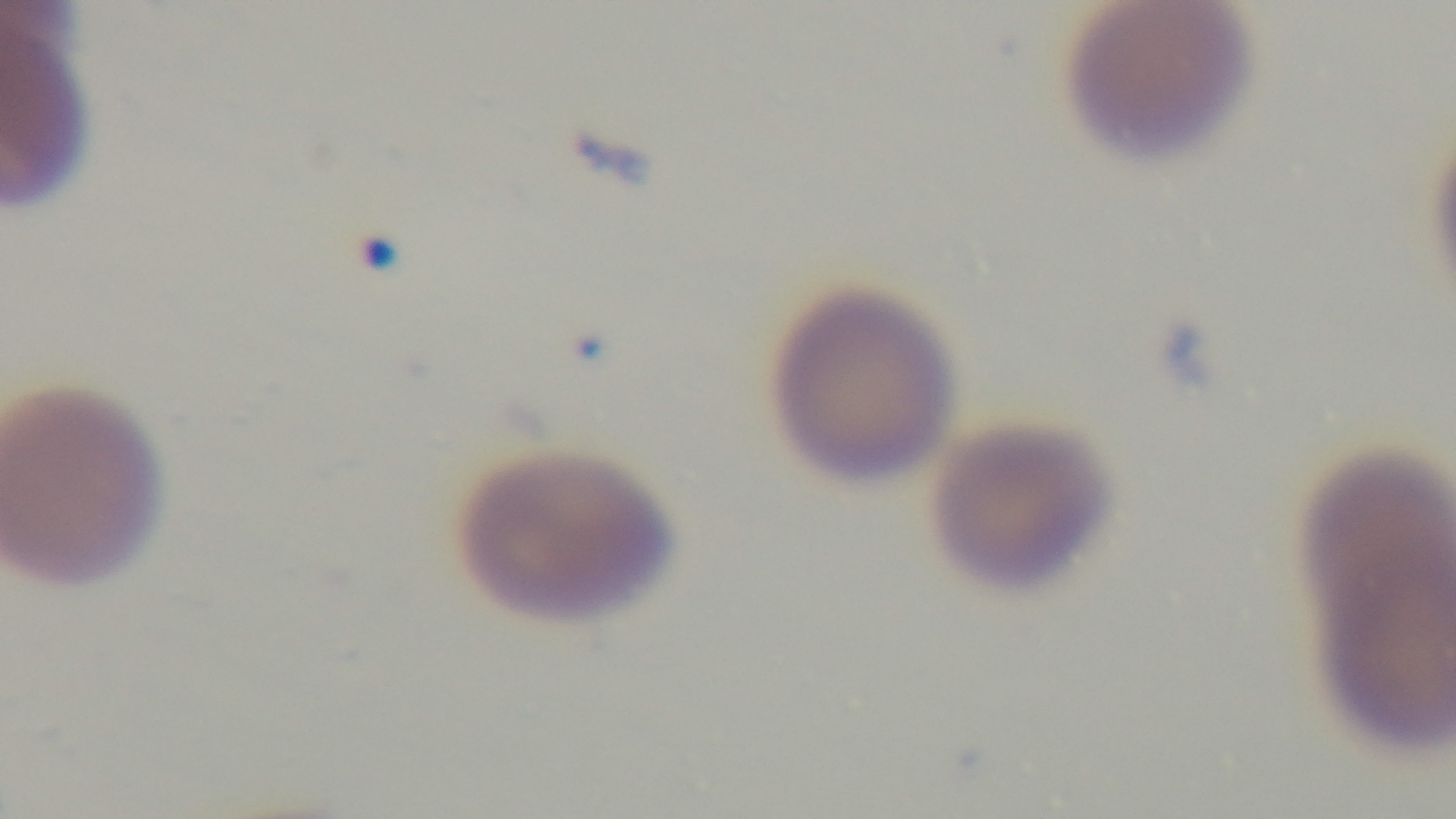
Summary:
  - Stain: Giemsa
  - Field of view: one from the slide
  - Malaria status: infected
  - Objective: 100x oil immersion
  - Preparation: thin
  - Modality: light microscopy
  - Capture: mounted 4K digital camera